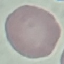
Malaria status: uninfected. Giemsa-stained preparation. Thin blood film. Acquired by smartphone through the microscope eyepiece. Automatically extracted cell patch, resized to 64 × 64 pixels.